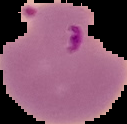
From a thin blood film. Image is 127×124 pixels. The area outside the segmented cell region is set to black. Malaria status: parasitized.